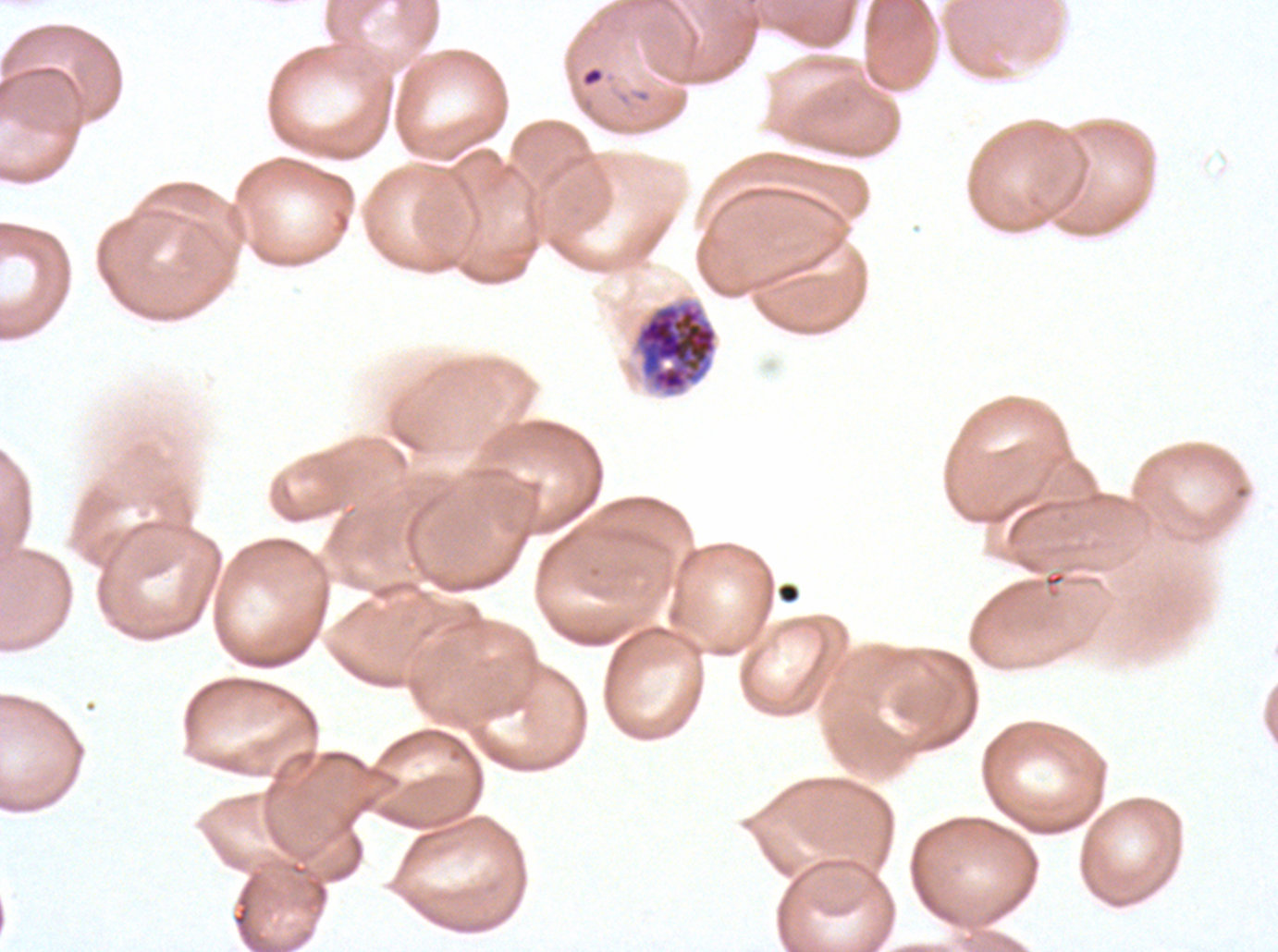
{
  "ring_locations": "approximate bounding boxes as [x1, y1, x2, y2] in pixels: [581, 66, 605, 87]",
  "early_schizont_locations": "approximate bounding boxes as [x1, y1, x2, y2] in pixels: [634, 301, 718, 394]",
  "stain": "Giemsa",
  "field_of_view": "one sub-image of a larger composite",
  "life_cycle_stages_observed": "ring, early schizont",
  "preparation": "thin blood smear",
  "specimen": "Plasmodium falciparum from a patient in The Gambia, cultured ex vivo for 24 to 48 hours",
  "image_size": "1278×952 pixels"
}